Classify this cell by malaria status.
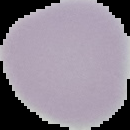

It is uninfected.

Image is 130×130 pixels. The area outside the segmented cell region is set to black. From a thin blood smear.